Name the parasite shown.
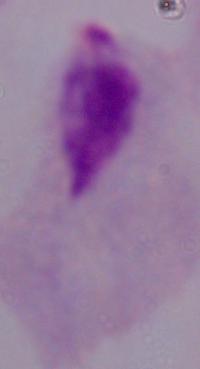

A trichomonad.

Summary:
  - Magnification: 1000x
  - Modality: micrograph